Comment on the morphology of the red blood cells.
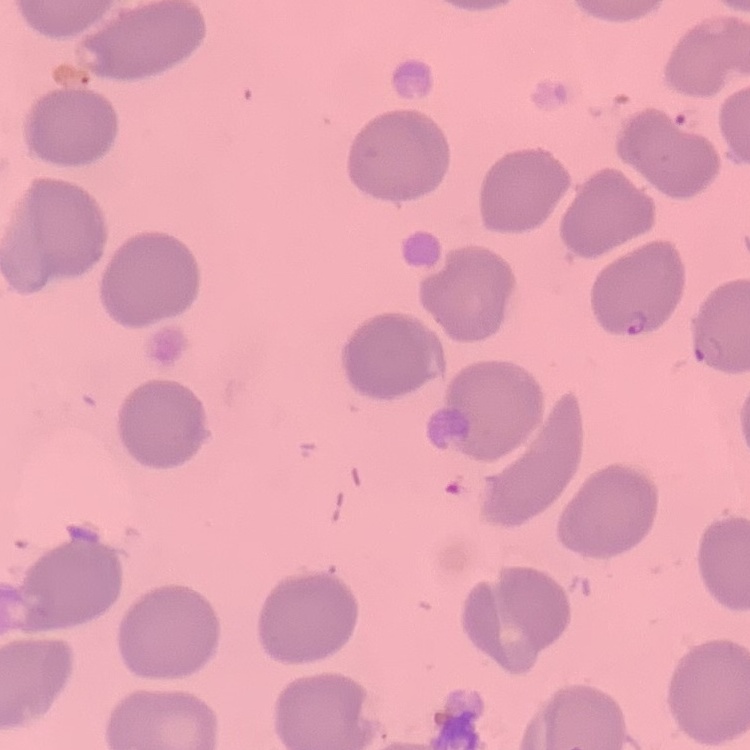
No rouleaux formation.

One tile cut from a larger photomicrograph. Field's or Giemsa stain. Thin blood smear.